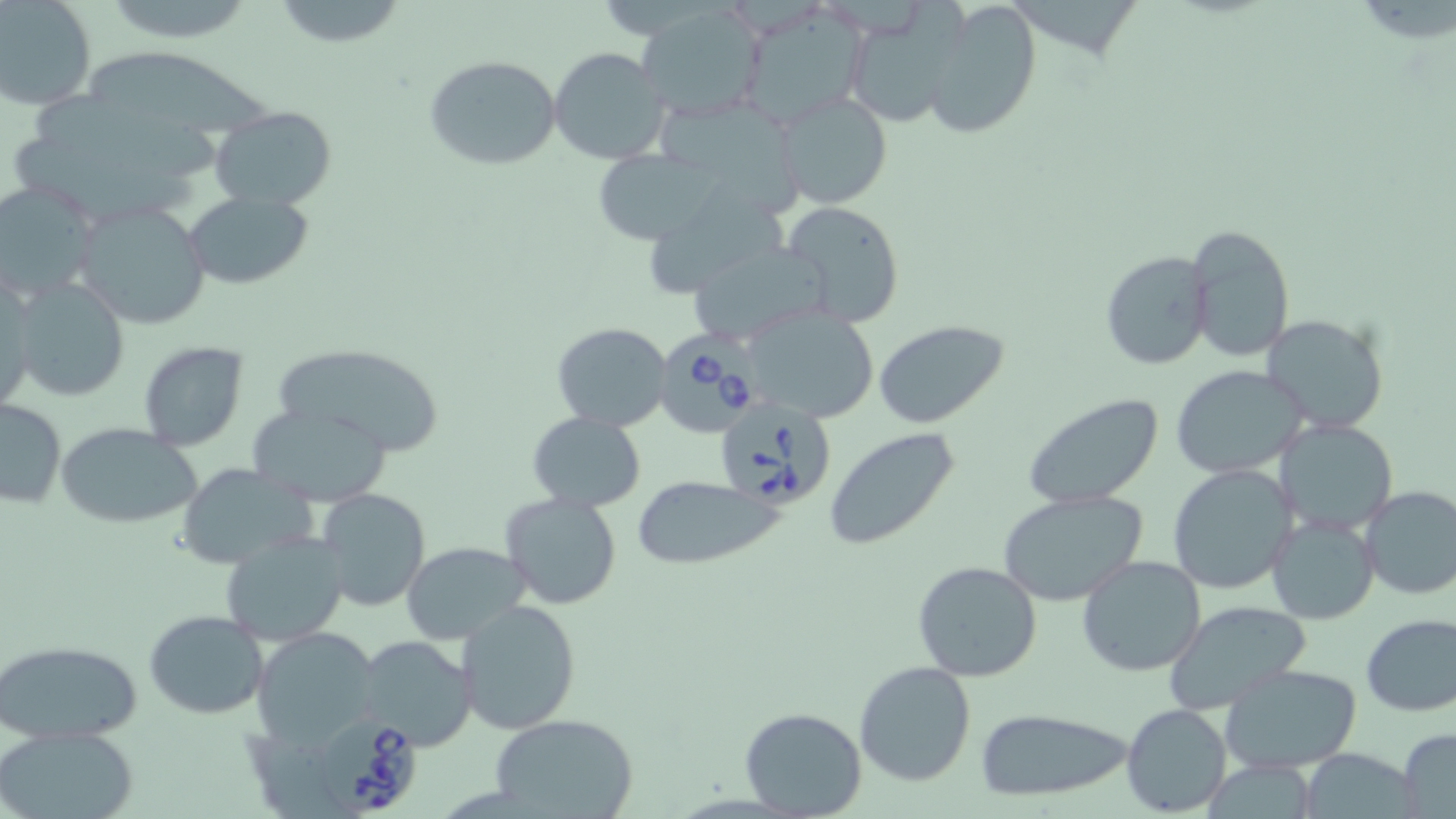

Summary:
  - Coordinate format: approximate bounding boxes as named x1/y1/x2/y2 corners in pixels
  - Babesia divergens-infected red blood cell locations: (x1=657, y1=332, x2=770, y2=442), (x1=712, y1=396, x2=836, y2=509), (x1=320, y1=720, x2=421, y2=818)
  - Uninfected red blood cell locations: (x1=0, y1=0, x2=96, y2=111), (x1=270, y1=0, x2=410, y2=50), (x1=920, y1=0, x2=1044, y2=141), (x1=115, y1=1, x2=252, y2=47), (x1=739, y1=2, x2=871, y2=127), (x1=635, y1=3, x2=768, y2=118), (x1=842, y1=7, x2=965, y2=127), (x1=549, y1=46, x2=672, y2=165), (x1=79, y1=51, x2=284, y2=140), (x1=425, y1=54, x2=563, y2=171), (x1=771, y1=90, x2=894, y2=211), (x1=34, y1=91, x2=228, y2=188), (x1=652, y1=99, x2=812, y2=214), (x1=209, y1=105, x2=336, y2=208), (x1=14, y1=138, x2=233, y2=224), (x1=591, y1=149, x2=731, y2=246), (x1=645, y1=174, x2=791, y2=297), (x1=0, y1=182, x2=101, y2=301), (x1=183, y1=192, x2=313, y2=289), (x1=780, y1=199, x2=906, y2=328), (x1=73, y1=201, x2=212, y2=330), (x1=1187, y1=221, x2=1297, y2=365), (x1=683, y1=240, x2=833, y2=346), (x1=1100, y1=249, x2=1213, y2=370), (x1=9, y1=273, x2=131, y2=404), (x1=0, y1=278, x2=39, y2=413), (x1=744, y1=306, x2=881, y2=423), (x1=1261, y1=314, x2=1389, y2=434), (x1=873, y1=320, x2=1009, y2=429), (x1=552, y1=322, x2=672, y2=431), (x1=137, y1=341, x2=250, y2=450), (x1=273, y1=342, x2=446, y2=456), (x1=1171, y1=365, x2=1312, y2=479), (x1=1022, y1=392, x2=1166, y2=508), (x1=0, y1=397, x2=65, y2=509), (x1=247, y1=403, x2=391, y2=505), (x1=526, y1=411, x2=647, y2=511), (x1=1273, y1=418, x2=1397, y2=535), (x1=58, y1=421, x2=202, y2=528), (x1=822, y1=429, x2=961, y2=550), (x1=174, y1=462, x2=319, y2=571), (x1=1168, y1=464, x2=1297, y2=595), (x1=632, y1=476, x2=780, y2=569), (x1=1357, y1=484, x2=1456, y2=599), (x1=315, y1=488, x2=431, y2=612), (x1=996, y1=489, x2=1149, y2=607), (x1=498, y1=491, x2=624, y2=611), (x1=1266, y1=514, x2=1380, y2=624), (x1=219, y1=530, x2=349, y2=646), (x1=402, y1=542, x2=530, y2=644), (x1=1077, y1=555, x2=1205, y2=677), (x1=911, y1=560, x2=1042, y2=683), (x1=457, y1=600, x2=582, y2=736), (x1=1162, y1=601, x2=1311, y2=717), (x1=143, y1=609, x2=270, y2=719), (x1=1359, y1=614, x2=1456, y2=717), (x1=254, y1=626, x2=379, y2=743), (x1=355, y1=636, x2=480, y2=751), (x1=1, y1=638, x2=143, y2=744), (x1=854, y1=662, x2=976, y2=787), (x1=1222, y1=663, x2=1363, y2=775), (x1=1121, y1=703, x2=1233, y2=815), (x1=739, y1=706, x2=868, y2=818), (x1=974, y1=706, x2=1137, y2=804), (x1=490, y1=714, x2=640, y2=819), (x1=0, y1=728, x2=141, y2=819), (x1=1395, y1=729, x2=1456, y2=818), (x1=1300, y1=747, x2=1418, y2=819), (x1=1201, y1=757, x2=1320, y2=819)
  - Slide-level diagnosis: Babesia divergens
  - Stain: May-Grünwald-Giemsa
  - Magnification: 1000x
  - Modality: optical microscopy
  - Image size: 1456×819 pixels
  - Preparation: thin blood smear
  - Field of view: single